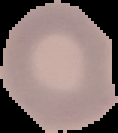

Summary:
  - Image size: 118×133 pixels
  - Image type: segmented cell region with the area outside set to black
  - Preparation: thin blood smear
  - Malaria status: uninfected